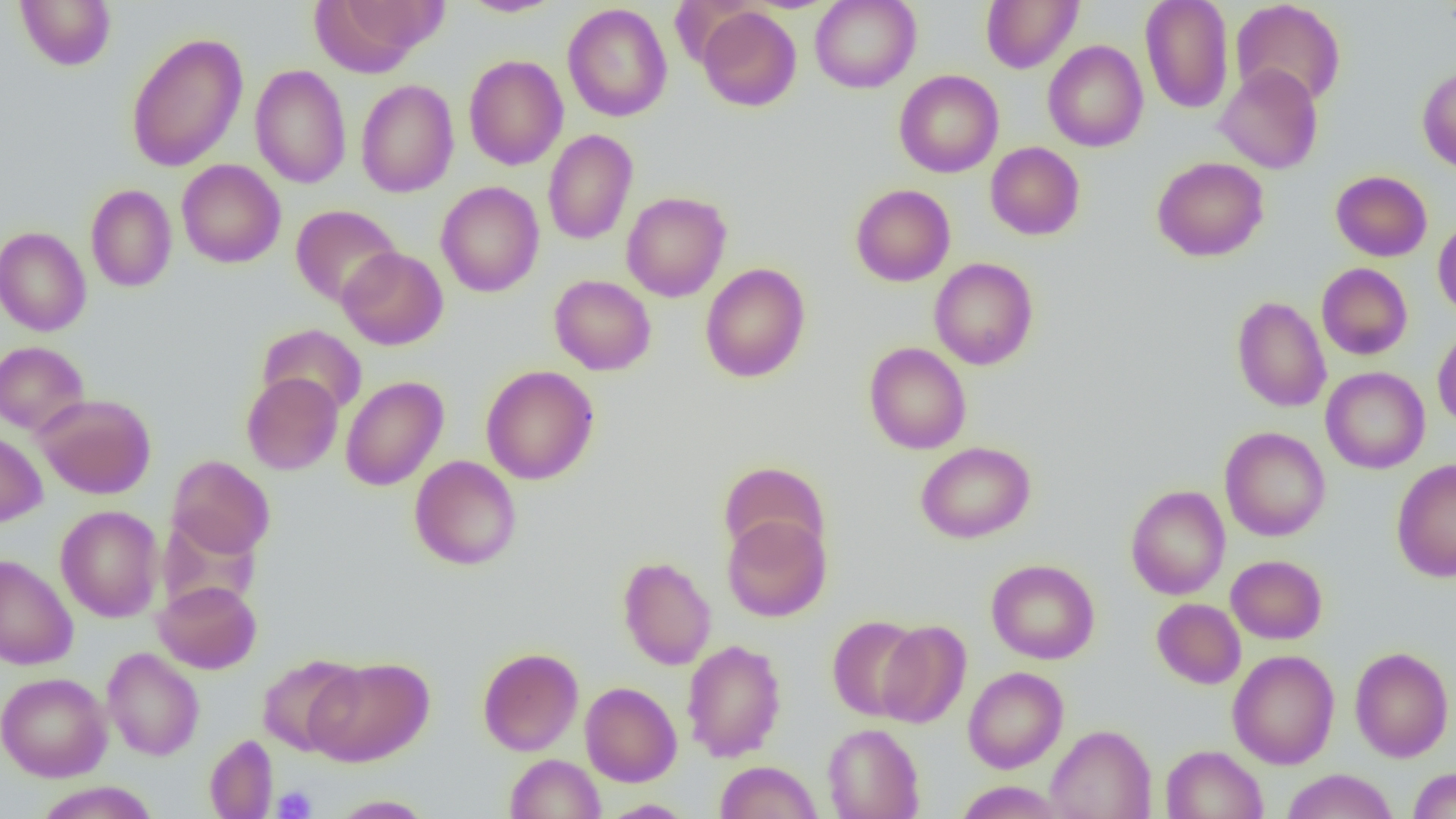

Summary:
  - Coordinate format: approximate bounding boxes as (x1, y1, x2, y2) in pixels
  - Platelet locations: (272, 785, 316, 818)
  - Uninfected red blood cell locations: (15, 0, 116, 71), (311, 0, 441, 75), (459, 0, 565, 17), (810, 0, 921, 93), (981, 0, 1083, 73), (1140, 0, 1234, 114), (1231, 0, 1346, 107), (563, 3, 673, 122), (697, 6, 801, 111), (125, 31, 248, 173), (1043, 40, 1148, 152), (463, 55, 568, 170), (1215, 64, 1323, 174), (250, 65, 351, 189), (1417, 65, 1456, 174), (894, 70, 1004, 177), (356, 79, 459, 198), (543, 129, 638, 245), (985, 142, 1085, 240), (1152, 157, 1269, 262), (177, 159, 285, 268), (1331, 170, 1432, 261), (436, 181, 544, 297), (85, 184, 177, 292), (850, 184, 955, 286), (621, 191, 731, 302), (290, 204, 403, 308), (1433, 219, 1456, 319), (0, 226, 91, 337), (338, 247, 448, 350), (929, 257, 1039, 370), (700, 263, 811, 383), (1317, 263, 1413, 360), (549, 275, 656, 375), (1232, 296, 1331, 412), (256, 324, 367, 418), (1432, 327, 1456, 430), (0, 341, 89, 435), (864, 342, 972, 454), (481, 365, 599, 485), (1321, 366, 1430, 473), (241, 372, 342, 475), (341, 376, 449, 491), (35, 393, 156, 499), (1219, 426, 1331, 542), (0, 429, 47, 528), (915, 441, 1035, 543), (167, 455, 275, 558), (409, 455, 522, 570), (1391, 458, 1456, 583), (718, 461, 830, 560), (1126, 485, 1230, 600), (55, 505, 164, 622), (155, 514, 262, 614), (722, 514, 832, 622), (0, 555, 78, 670), (1226, 555, 1327, 644), (617, 556, 716, 670), (986, 559, 1100, 664), (153, 579, 262, 674), (1152, 598, 1246, 689), (826, 615, 925, 721), (875, 620, 971, 728), (681, 639, 787, 762), (1349, 646, 1454, 762), (102, 647, 204, 761), (477, 647, 583, 756), (1227, 649, 1340, 769), (257, 654, 362, 755), (305, 657, 434, 766), (963, 666, 1069, 772), (0, 672, 112, 782), (580, 682, 682, 787), (822, 723, 925, 819), (1046, 724, 1156, 819), (204, 734, 278, 818), (1161, 744, 1268, 819), (505, 753, 605, 818), (714, 760, 822, 819), (1407, 767, 1456, 819), (1281, 768, 1398, 819), (33, 781, 161, 819), (955, 781, 1066, 818), (329, 795, 436, 818), (597, 799, 696, 818)
  - Slide-level diagnosis: no evidence of blood parasites
  - Preparation: thin blood film
  - Magnification: 1000x
  - Image size: 1456×819 pixels
  - Modality: optical microscopy
  - Field of view: one of a larger specimen